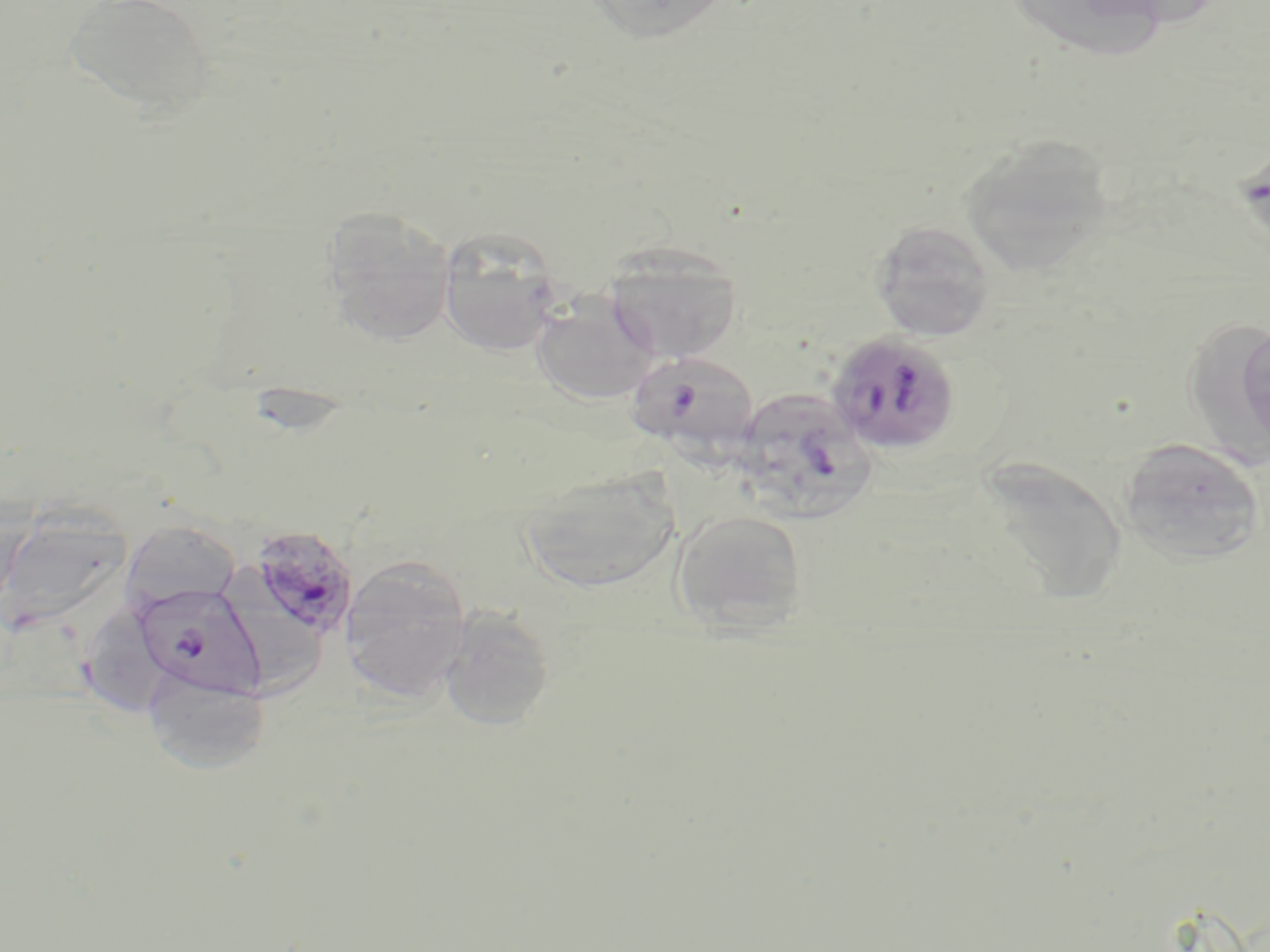 Approximate bounding boxes as (x1,y1)-(x2,y2) corner pairs in pixels. Uninfected red blood cell locations: (63,0)-(218,118), (585,0)-(733,43), (1016,0)-(1168,74), (959,135)-(1116,278), (321,206)-(458,346), (869,218)-(998,342), (436,225)-(565,356), (601,242)-(743,363), (529,293)-(660,407), (1187,313)-(1270,487), (1236,318)-(1270,454), (1118,437)-(1267,567), (968,456)-(1128,607), (517,468)-(681,595), (0,508)-(132,633), (670,509)-(810,635), (120,520)-(241,613), (341,554)-(472,703), (225,563)-(330,698), (71,602)-(177,721), (438,605)-(556,730), (141,664)-(272,776). Plasmodium falciparum-infected red blood cell locations: (825,331)-(961,456), (625,349)-(760,456), (731,387)-(878,521), (249,524)-(358,640), (133,583)-(265,698). Slide-level diagnosis: Plasmodium falciparum. Captured at 1000x magnification. Optical microscopy. One field of a larger specimen. Thin blood smear. May-Grünwald-Giemsa stain. Image is 1270×952 pixels.